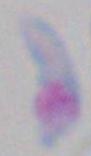
Summary:
  - Identification: Toxoplasma gondii
  - Magnification: 1000x
  - Modality: micrograph